State which parasite is depicted.
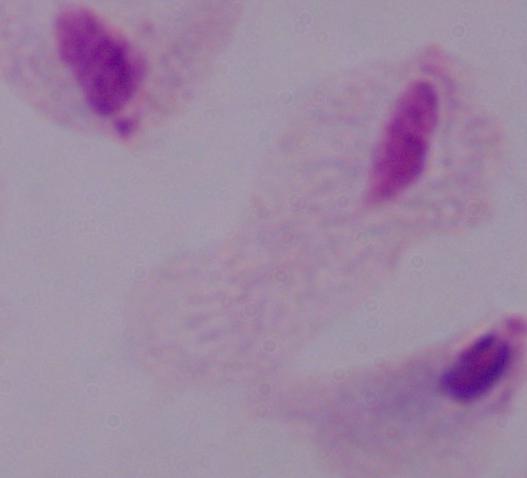
A trichomonad.

Summary:
  - Magnification: 1000x
  - Modality: photomicrograph